Classify this cell by malaria status.
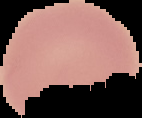

Uninfected.

Summary:
  - Preparation: thin blood film
  - Image size: 142×118 pixels
  - Image type: segmented cell region with the area outside set to black